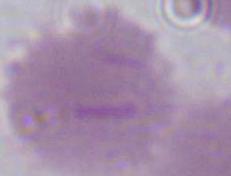

Summary:
  - Magnification: 1000x
  - Identification: erythrocyte
  - Modality: photomicrograph